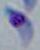

Summary:
  - Identification: Toxoplasma gondii
  - Magnification: 1000x
  - Modality: micrograph